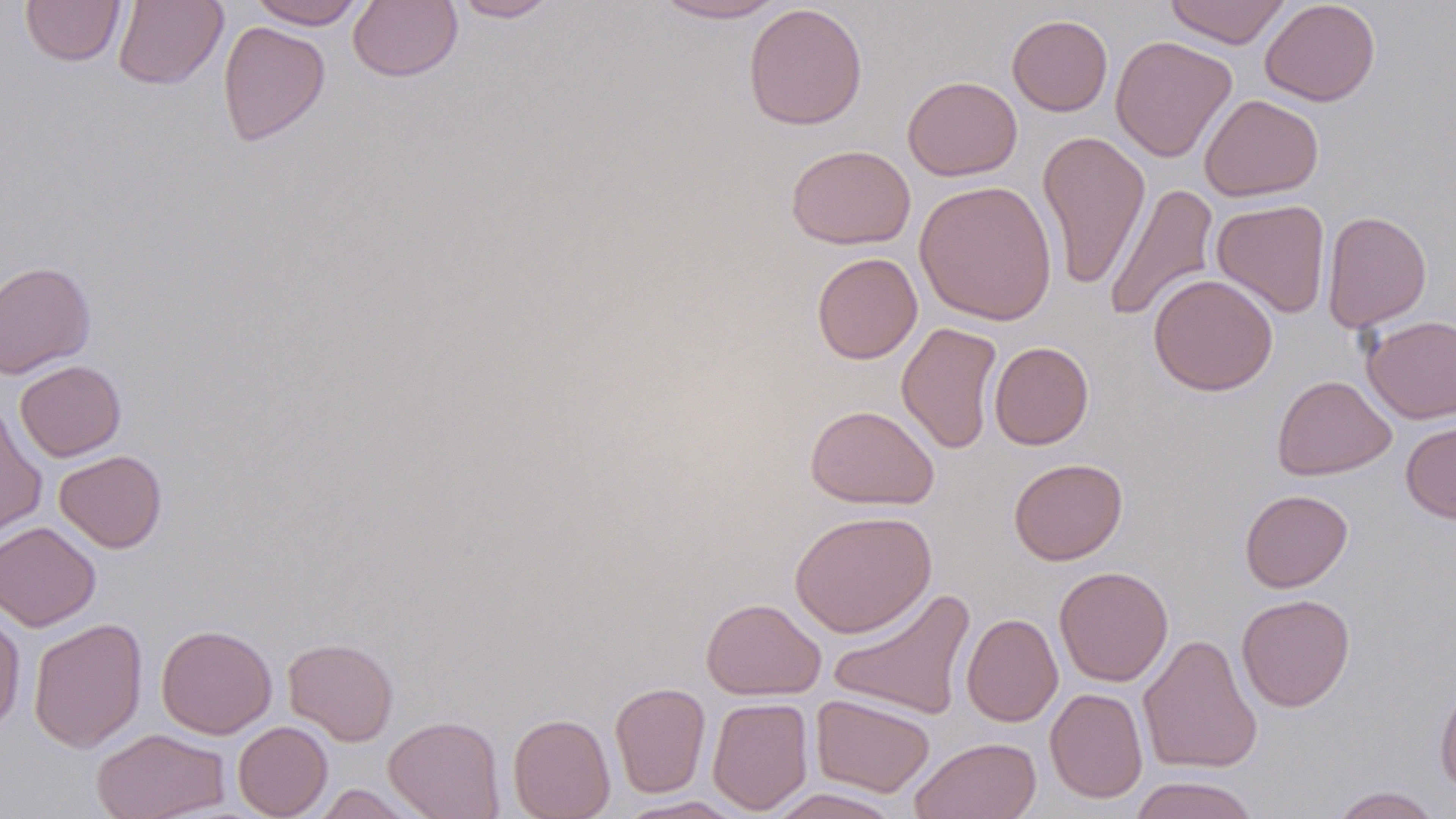

Approximate bounding boxes as (x1,y1)-(x2,y2) corner pairs in pixels. Uninfected red blood cell locations: (20,0)-(125,67), (113,0)-(228,90), (248,0)-(366,29), (450,0)-(561,22), (652,0)-(787,23), (1164,0)-(1291,49), (1259,0)-(1381,106), (348,1)-(463,82), (743,3)-(868,130), (1007,14)-(1113,116), (217,21)-(330,147), (1110,35)-(1237,163), (902,75)-(1022,181), (1199,94)-(1324,201), (1037,129)-(1151,290), (786,144)-(916,250), (914,179)-(1058,325), (1103,182)-(1219,324), (1212,199)-(1331,318), (1321,210)-(1431,333), (811,252)-(923,364), (0,260)-(96,378), (1148,274)-(1278,396), (1360,315)-(1456,423), (896,322)-(1003,454), (989,341)-(1093,450), (14,360)-(127,462), (1271,375)-(1396,480), (0,401)-(48,542), (804,404)-(940,510), (1400,417)-(1456,523), (54,450)-(167,553), (1008,458)-(1128,565), (1239,489)-(1353,593), (789,510)-(937,638), (0,521)-(101,631), (1054,566)-(1173,687), (828,587)-(976,720), (1236,594)-(1355,711), (701,597)-(825,700), (0,608)-(26,733), (961,612)-(1062,727), (28,617)-(148,753), (156,624)-(277,739), (1138,633)-(1263,774), (283,637)-(399,746), (1434,670)-(1456,794), (609,682)-(711,798), (1045,687)-(1148,803), (811,693)-(935,797), (707,696)-(814,815), (508,713)-(616,819), (384,715)-(505,818), (233,721)-(333,818), (91,727)-(231,819), (909,736)-(1042,819), (1127,775)-(1262,819), (312,784)-(419,818), (1329,786)-(1443,819), (765,788)-(905,818), (615,795)-(747,818). Slide-level diagnosis: negative for blood parasites. Light microscopy. Captured at 1000x magnification. One field of a larger specimen. May-Grünwald-Giemsa-stained preparation. Image is 1456×819 pixels. Thin blood film.